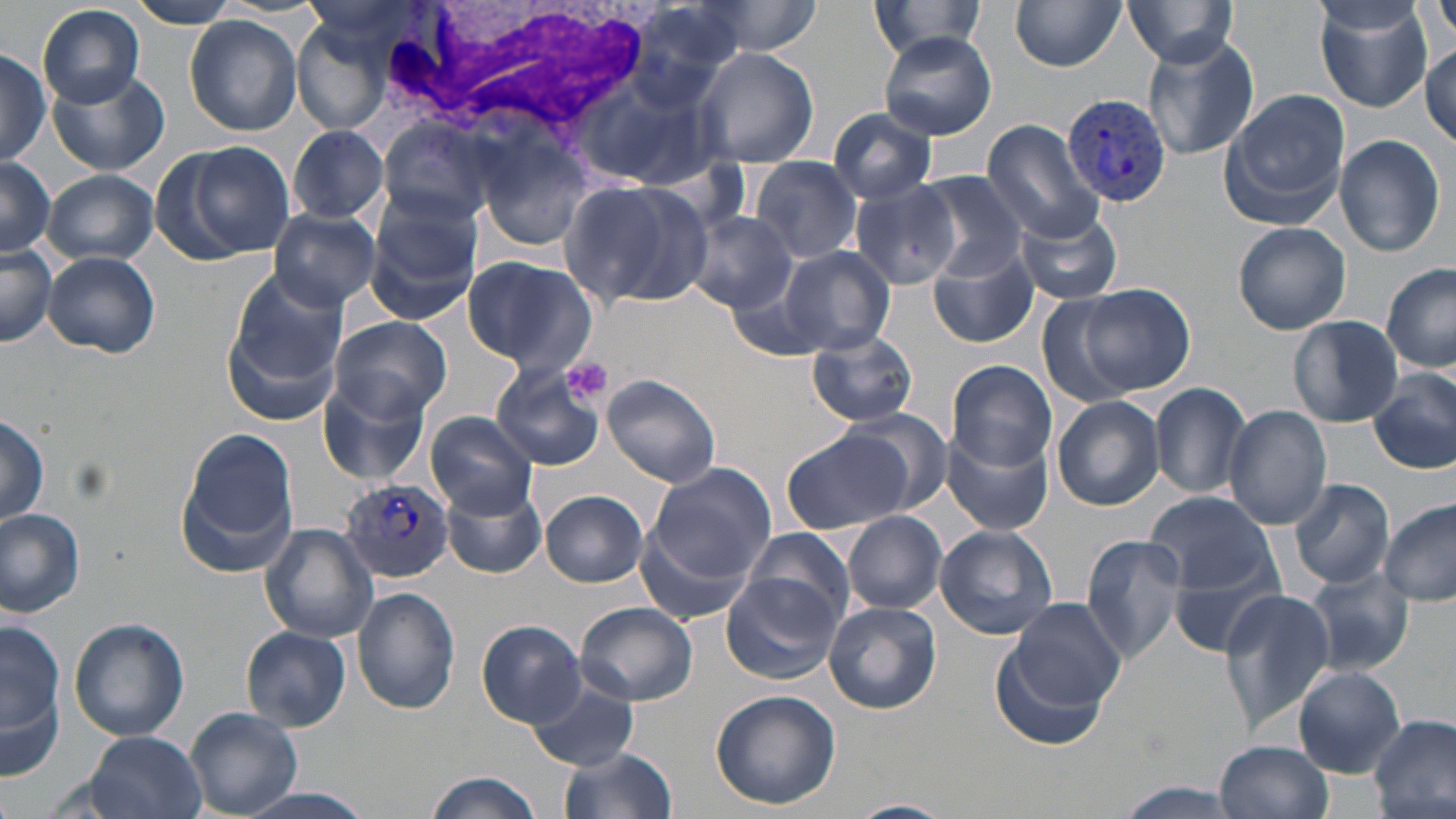
Summary:
  - Coordinate format: approximate bounding boxes as (x1,y1)-(x2,y2) corner pairs in pixels
  - White blood cell locations: (380,2)-(660,148)
  - Plasmodium vivax-infected red blood cell locations: (1062,94)-(1174,207), (340,476)-(457,583)
  - Platelet locations: (560,356)-(612,404)
  - Uninfected red blood cell locations: (869,0)-(990,63), (1009,0)-(1126,71), (1312,0)-(1435,112), (1428,0)-(1456,47), (125,1)-(245,28), (1124,1)-(1238,69), (37,4)-(146,109), (184,15)-(303,136), (296,25)-(382,130), (878,32)-(996,139), (1138,33)-(1260,161), (1421,35)-(1454,147), (0,45)-(48,165), (693,46)-(817,168), (46,68)-(169,176), (1220,89)-(1349,228), (826,106)-(939,203), (981,119)-(1105,244), (379,120)-(499,228), (288,124)-(388,225), (478,130)-(600,254), (1333,134)-(1446,257), (165,140)-(296,263), (0,153)-(56,260), (750,157)-(862,265), (42,169)-(158,267), (914,173)-(1029,280), (562,179)-(713,311), (848,181)-(962,293), (365,193)-(482,322), (268,207)-(380,310), (1012,207)-(1123,305), (684,212)-(799,313), (1233,220)-(1352,335), (0,243)-(56,347), (930,245)-(1040,350), (780,248)-(894,358), (43,250)-(160,357), (462,255)-(597,376), (1382,263)-(1456,374), (725,265)-(831,356), (223,275)-(347,423), (1067,282)-(1195,399), (1036,292)-(1144,409), (328,315)-(452,421), (1287,315)-(1404,427), (808,331)-(919,426), (948,360)-(1057,471), (490,363)-(606,471), (1370,369)-(1456,476), (602,374)-(722,490), (318,377)-(432,484), (1150,382)-(1252,500), (1052,394)-(1164,512), (1224,405)-(1333,531), (842,409)-(953,513), (425,411)-(538,516), (0,413)-(49,527), (177,427)-(300,575), (941,428)-(1055,537), (781,429)-(913,535), (641,462)-(775,599), (1290,478)-(1394,588), (444,486)-(546,579), (540,490)-(649,587), (1146,490)-(1277,594), (1380,500)-(1455,606), (0,509)-(86,617), (842,511)-(947,614), (258,523)-(380,642), (934,524)-(1059,640), (740,526)-(856,627), (1081,532)-(1192,661), (1168,548)-(1291,656), (1280,562)-(1407,770), (1302,567)-(1416,676), (722,573)-(842,685), (352,587)-(460,717), (1219,587)-(1337,733), (1003,595)-(1129,714), (824,601)-(942,713), (576,602)-(697,705), (3,616)-(68,771), (68,617)-(189,742), (478,620)-(587,726), (243,627)-(353,731), (992,635)-(1114,752), (1294,665)-(1406,776), (528,678)-(641,770), (709,689)-(840,810), (186,706)-(304,817), (1370,715)-(1456,816), (82,732)-(209,819), (1215,740)-(1334,819), (557,745)-(679,819), (424,771)-(545,819), (1108,783)-(1253,816), (844,798)-(957,819)
  - Slide-level diagnosis: Plasmodium vivax
  - Preparation: thin blood film
  - Magnification: 1000x
  - Stain: May-Grünwald-Giemsa
  - Field of view: single
  - Modality: optical microscopy
  - Image size: 1456×819 pixels